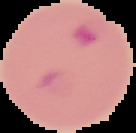
Summary:
  - Image size: 136×133 pixels
  - Image type: segmented cell region with the area outside set to black
  - Preparation: thin blood smear
  - Malaria status: parasitized